Locate every Plasmodium parasite.
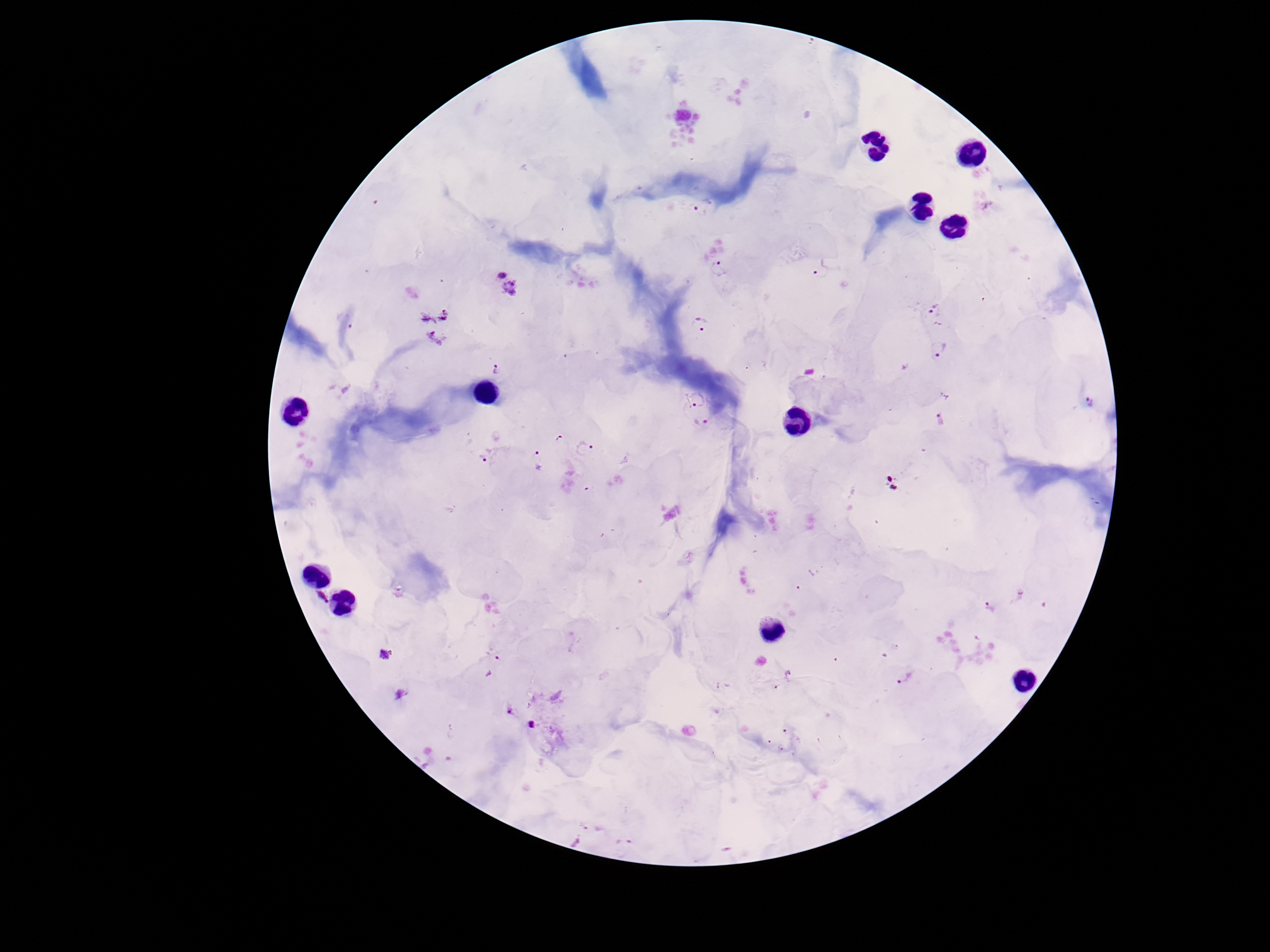
Approximate object centers, in pixels from the top-left corner.
Plasmodium parasites: (x=702, y=208), (x=718, y=268), (x=821, y=271), (x=500, y=274), (x=513, y=288), (x=935, y=309), (x=701, y=326), (x=938, y=348), (x=496, y=368), (x=696, y=398), (x=1091, y=402), (x=940, y=420), (x=701, y=423), (x=585, y=449), (x=485, y=454), (x=538, y=459), (x=322, y=596), (x=991, y=606), (x=384, y=655), (x=788, y=673), (x=904, y=677), (x=401, y=694), (x=510, y=711), (x=531, y=724).

Summary:
  - Patient malaria status: infected
  - Stain: Giemsa
  - Preparation: thick blood smear
  - Field of view: single
  - Capture: smartphone camera through the microscope eyepiece
  - Image size: 1270×952 pixels
  - Magnification: 100x